Assess this cell for malaria.
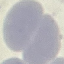

It is uninfected.

Giemsa-stained preparation. Photographed with a smartphone camera at the microscope eyepiece. Cell patch, automatically extracted from a larger field of view and resized to 64 × 64 pixels. Thin blood smear.